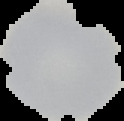

result = no Plasmodium parasites seen
image size = 124×121 pixels
image type = segmented cell region on a black background
preparation = thin blood film